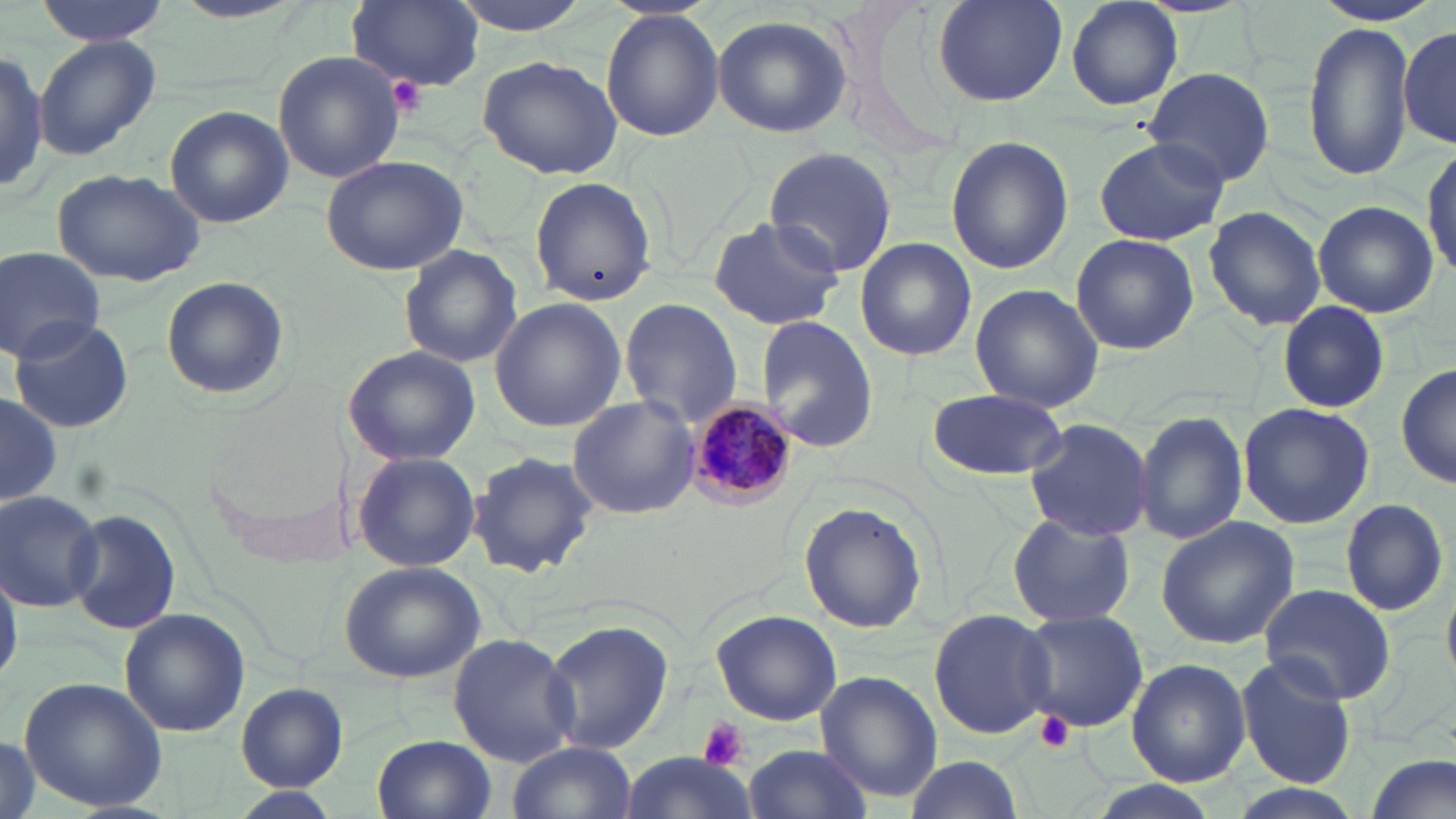 Approximate bounding boxes as (x1,y1)-(x2,y2) corner pairs in pixels. Uninfected red blood cell locations: (33,0)-(170,44), (447,0)-(600,34), (928,0)-(1070,106), (1062,0)-(1185,111), (346,1)-(485,92), (1307,1)-(1449,26), (599,11)-(724,141), (711,14)-(853,139), (1302,22)-(1417,181), (1399,28)-(1456,146), (33,35)-(160,161), (0,45)-(46,199), (274,51)-(405,185), (478,52)-(625,179), (1141,66)-(1276,188), (166,107)-(294,228), (945,132)-(1072,273), (1094,137)-(1229,246), (1424,144)-(1456,283), (763,146)-(896,278), (320,153)-(468,277), (50,168)-(206,286), (529,178)-(656,302), (1312,200)-(1437,318), (1203,205)-(1326,329), (708,216)-(842,330), (1069,234)-(1200,355), (855,237)-(977,362), (399,246)-(521,369), (1,248)-(106,361), (159,274)-(291,400), (970,283)-(1104,413), (489,298)-(627,432), (620,299)-(742,431), (1278,302)-(1389,415), (755,315)-(878,452), (8,317)-(136,434), (342,346)-(480,464), (1396,358)-(1455,491), (925,387)-(1066,481), (0,391)-(61,512), (566,395)-(701,521), (1236,401)-(1377,531), (1133,410)-(1247,546), (1022,416)-(1153,541), (351,450)-(482,573), (467,450)-(601,578), (0,489)-(104,611), (1339,496)-(1448,616), (799,501)-(927,635), (66,506)-(182,635), (1007,513)-(1135,630), (1155,515)-(1302,649), (339,559)-(485,682), (0,561)-(21,690), (1260,583)-(1395,703), (119,609)-(251,737), (709,609)-(843,727), (928,609)-(1058,739), (1017,609)-(1149,733), (542,620)-(673,756), (447,632)-(580,766), (1236,656)-(1356,790), (1126,657)-(1252,788), (816,671)-(942,802), (19,675)-(167,815), (234,683)-(350,791), (0,734)-(39,819), (373,734)-(498,819), (507,741)-(637,819), (744,742)-(871,819), (1364,751)-(1453,819), (617,754)-(758,819), (904,756)-(1026,817), (1077,784)-(1226,819). Platelet locations: (384,75)-(428,117), (1036,711)-(1075,752), (696,717)-(749,775). Plasmodium malariae-infected red blood cell locations: (689,399)-(801,506). Slide-level diagnosis: Plasmodium malariae. Image is 1456×819 pixels. Light microscopy. One field of a larger specimen. May-Grünwald-Giemsa-stained preparation. Thin blood film. Captured at 1000x magnification.